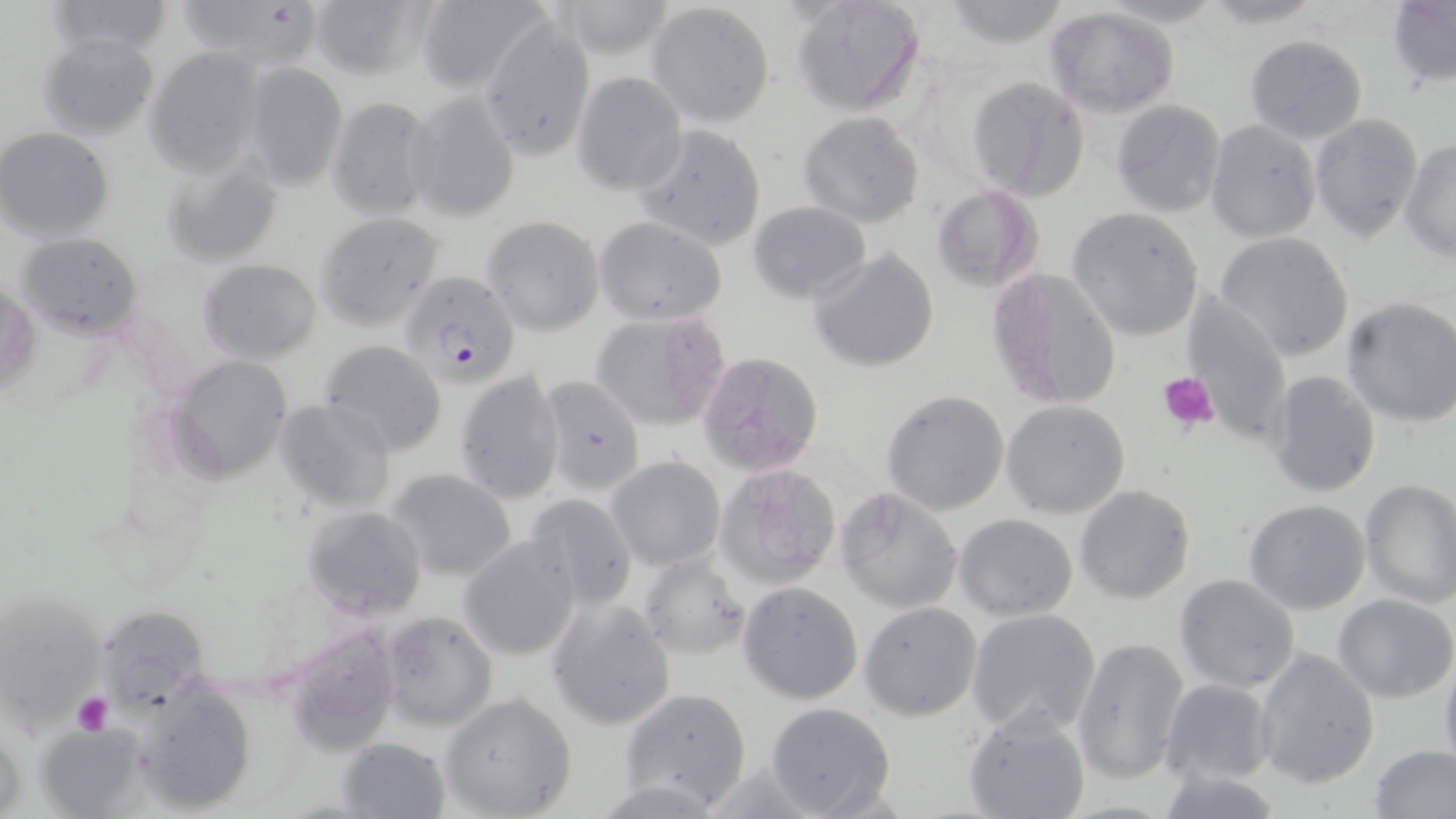
Approximate bounding boxes as [x1, y1, x2, y2] in pixels. Platelet locations: [1157, 369, 1220, 431], [71, 693, 114, 734]. Uninfected red blood cell locations: [42, 0, 174, 59], [181, 0, 318, 66], [309, 0, 435, 83], [553, 0, 682, 62], [791, 0, 927, 117], [932, 0, 1074, 50], [1192, 0, 1333, 28], [415, 1, 550, 96], [1387, 1, 1455, 89], [647, 2, 775, 127], [1045, 7, 1181, 118], [478, 13, 597, 163], [36, 33, 161, 138], [1242, 35, 1368, 143], [144, 46, 266, 175], [241, 60, 348, 191], [570, 72, 688, 195], [968, 76, 1089, 201], [407, 89, 521, 222], [325, 95, 438, 221], [1109, 99, 1228, 218], [797, 111, 925, 228], [1310, 114, 1424, 245], [1205, 120, 1322, 243], [631, 124, 768, 251], [1, 128, 117, 241], [1400, 141, 1455, 265], [161, 154, 286, 267], [931, 185, 1044, 295], [748, 200, 870, 300], [1068, 207, 1205, 340], [314, 212, 446, 329], [482, 216, 605, 334], [594, 216, 729, 327], [16, 231, 143, 337], [1214, 231, 1355, 362], [807, 248, 941, 374], [197, 258, 324, 363], [986, 267, 1124, 412], [1, 281, 38, 399], [1181, 288, 1293, 440], [1339, 298, 1456, 427], [588, 310, 732, 433], [318, 340, 448, 456], [695, 351, 825, 477], [167, 353, 294, 482], [454, 370, 566, 503], [1266, 370, 1382, 497], [540, 375, 647, 496], [880, 389, 1011, 517], [276, 400, 398, 514], [1001, 400, 1131, 518], [607, 456, 724, 570], [715, 463, 841, 590], [386, 468, 518, 581], [1359, 477, 1456, 607], [1074, 485, 1196, 604], [833, 487, 963, 613], [522, 493, 638, 610], [1242, 498, 1371, 615], [301, 505, 428, 619], [953, 513, 1079, 622], [459, 534, 581, 662], [638, 551, 753, 660], [1174, 574, 1302, 694], [738, 581, 863, 704], [2, 585, 116, 735], [1333, 595, 1456, 704], [546, 597, 676, 732], [96, 602, 213, 713], [859, 602, 981, 721], [965, 608, 1101, 738], [378, 610, 497, 732], [287, 623, 404, 751], [1070, 635, 1190, 788], [1255, 647, 1381, 788], [1439, 651, 1456, 777], [1160, 678, 1274, 786], [132, 683, 259, 813], [615, 687, 753, 811], [438, 692, 578, 818], [764, 701, 898, 819], [963, 706, 1092, 819], [0, 712, 26, 817], [36, 722, 150, 818], [336, 736, 451, 818], [1370, 744, 1456, 819], [1157, 764, 1285, 819]. Plasmodium falciparum-infected red blood cell locations: [397, 270, 522, 393]. Slide-level diagnosis: Plasmodium falciparum. May-Grünwald-Giemsa-stained preparation. Captured at 1000x magnification. Image is 1456×819 pixels. Optical microscopy. Single field of view. Thin blood film.